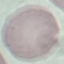

result = no malaria parasites detected
stain = Giemsa
preparation = thin blood film
image type = cell patch, automatically extracted from a larger field of view and resized to 64 × 64 pixels
capture = smartphone camera at the microscope eyepiece